Report the malaria status of this cell.
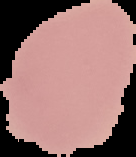
Uninfected.

Image is 136×157 pixels. From a thin blood film. Cell region segmented out of the field of view; the surrounding area is masked to black.